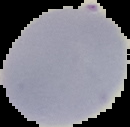
Summary:
  - Image type: cell region segmented out of the field of view; surrounding area masked to black
  - Result: no Plasmodium parasites seen
  - Preparation: thin blood smear
  - Image size: 130×127 pixels